Assess this cell for malaria.
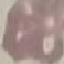

Uninfected.

Acquired by smartphone through the microscope eyepiece. Thin smear of blood. Giemsa stain. Automatically extracted cell patch, resized to 64 × 64 pixels.